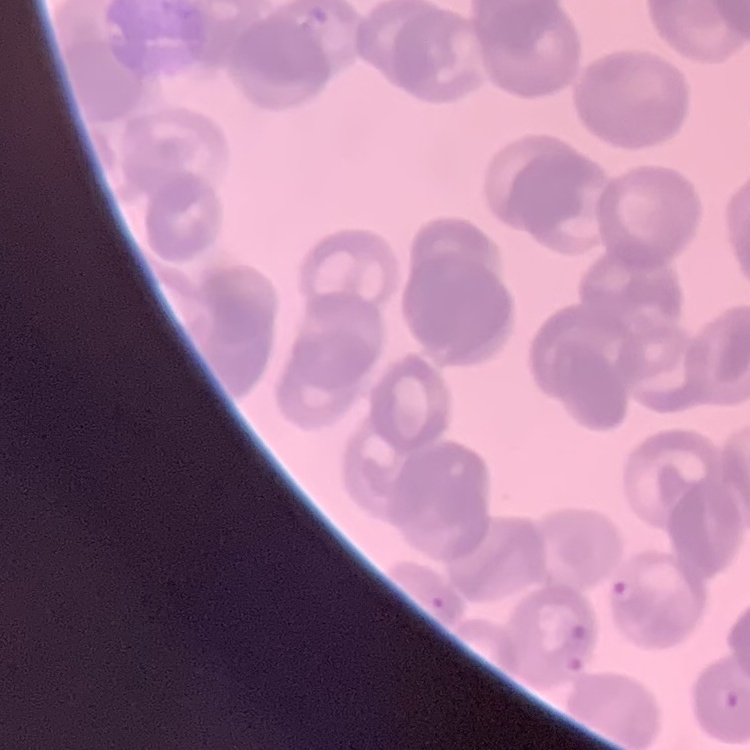

Summary:
  - Red blood cell morphology: rouleaux formation
  - Stain: Field's or Giemsa
  - Preparation: thin blood film
  - Image type: one tile cut from a larger photomicrograph